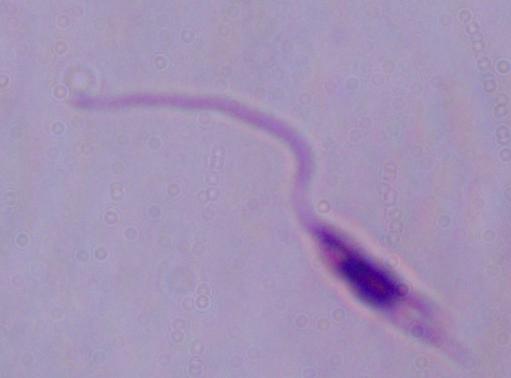

A Leishmania parasite is seen. Micrograph. Captured at 1000x magnification.